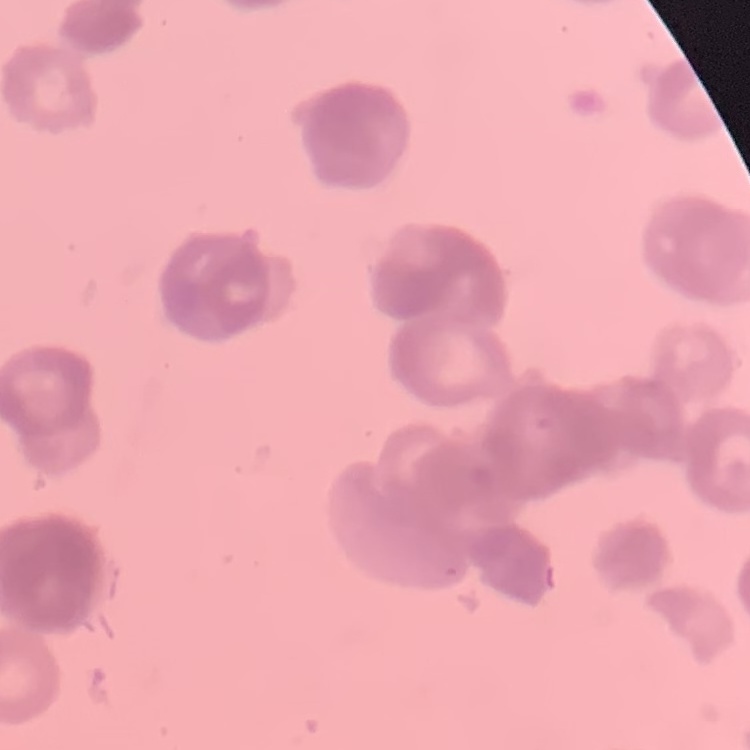 The red blood cells exhibit rouleaux formation. Field's or Giemsa stain. Square crop of a larger photomicrograph. Thin blood smear.